Assess this cell for malaria.
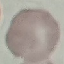

Uninfected.

image type = automatically extracted cell patch, resized to 64 × 64 pixels
stain = Giemsa
preparation = thin smear
capture = smartphone through the microscope eyepiece